Locate every leukocyte (white blood cell).
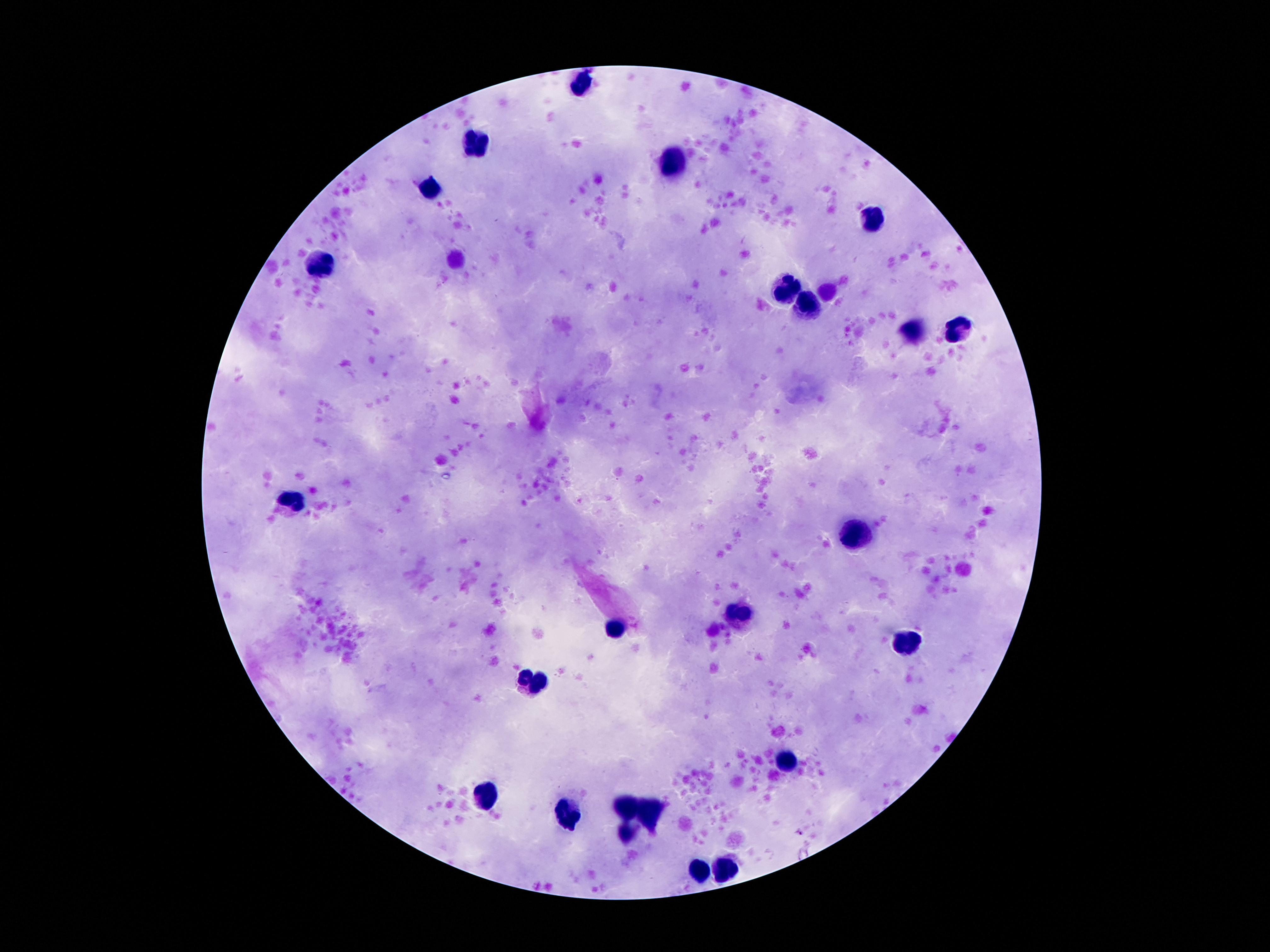

Approximate object centers, in pixels from the top-left corner.
Leukocytes: (x=579, y=85), (x=472, y=148), (x=673, y=166), (x=434, y=190), (x=873, y=215), (x=323, y=268), (x=787, y=288), (x=808, y=307), (x=909, y=331), (x=959, y=331), (x=289, y=506), (x=858, y=537), (x=738, y=614), (x=610, y=628), (x=902, y=647), (x=531, y=684), (x=785, y=760), (x=486, y=800), (x=627, y=807), (x=564, y=813), (x=652, y=813), (x=625, y=835), (x=701, y=867), (x=724, y=867).

Summary:
  - Image size: 1270×952 pixels
  - Field of view: single
  - Stain: Giemsa
  - Patient malaria status: negative
  - Magnification: 100x
  - Preparation: thick blood smear
  - Capture: smartphone camera through the microscope eyepiece